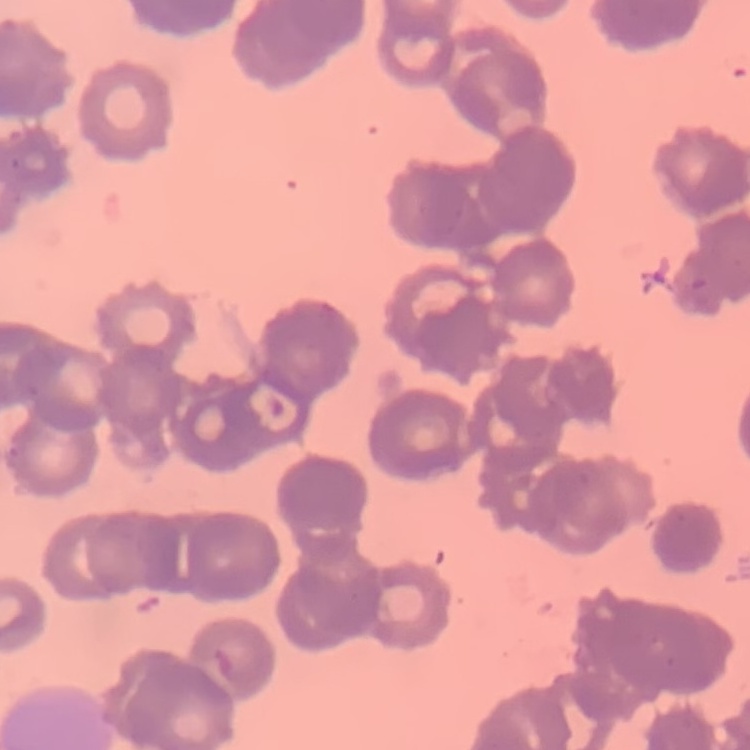 The erythrocytes exhibit rouleaux formation. Thin blood smear. Square crop of a larger photomicrograph. Field's or Giemsa stain.